Report the malaria status of this cell.
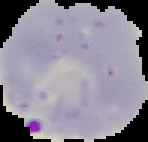
Parasitized.

preparation = thin blood smear
image size = 148×142 pixels
image type = segmented cell region with the area outside set to black